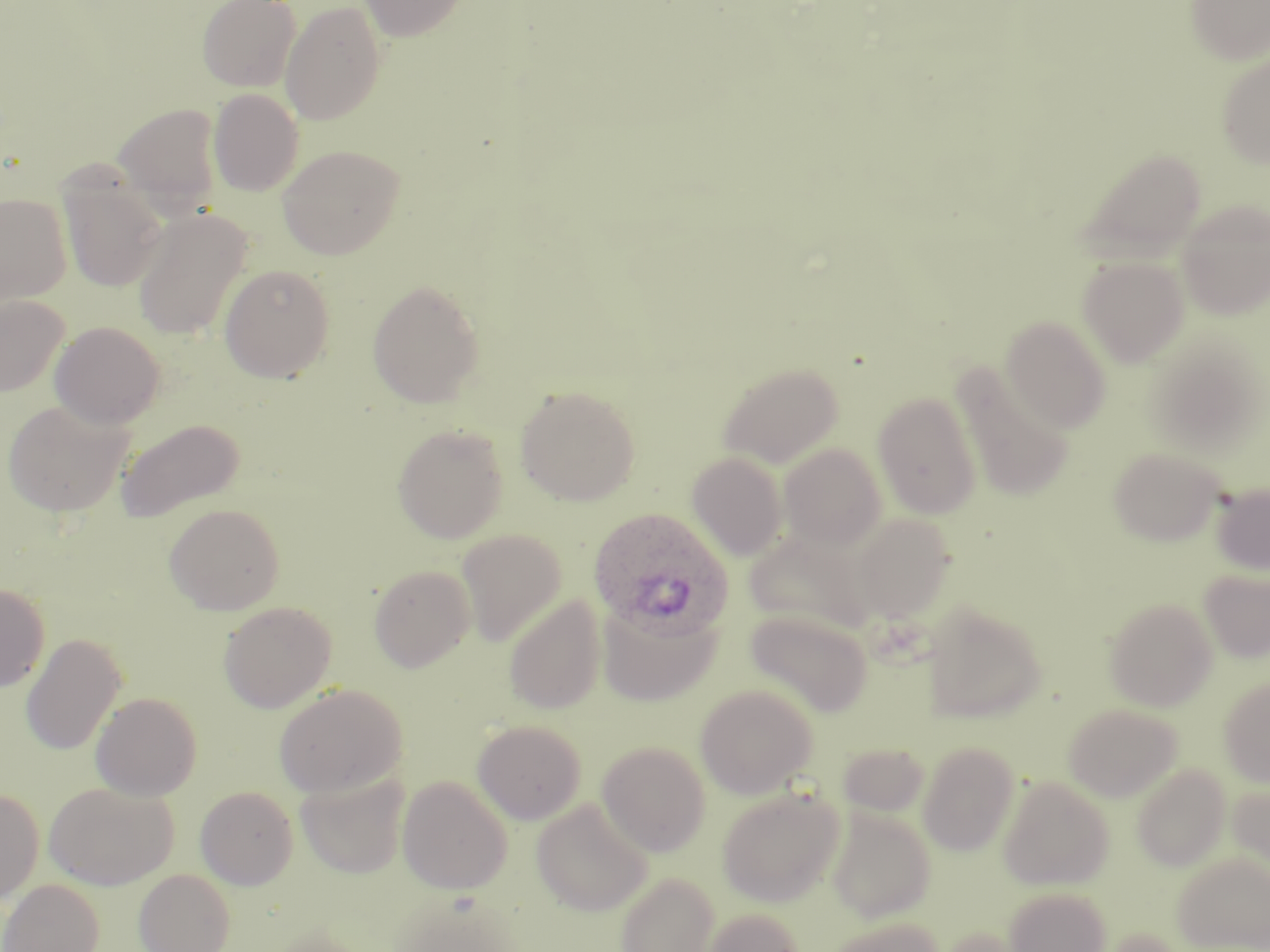

Summary:
  - Coordinate format: approximate bounding boxes as (x1, y1, x2, y2) in pixels
  - Uninfected red blood cell locations: (197, 0, 301, 91), (359, 0, 469, 41), (1185, 0, 1270, 65), (280, 1, 386, 125), (1216, 51, 1270, 169), (208, 89, 304, 196), (112, 102, 224, 212), (278, 144, 406, 259), (1076, 147, 1207, 262), (59, 174, 167, 293), (0, 193, 72, 305), (1177, 199, 1269, 320), (132, 208, 251, 341), (1078, 256, 1189, 367), (219, 263, 335, 382), (367, 279, 485, 407), (0, 294, 69, 396), (1002, 316, 1111, 433), (50, 321, 165, 429), (717, 361, 844, 469), (951, 361, 1074, 502), (515, 384, 640, 506), (873, 392, 981, 519), (2, 400, 135, 518), (115, 418, 245, 523), (392, 425, 508, 543), (779, 443, 887, 549), (1109, 446, 1226, 546), (686, 451, 787, 560), (1211, 482, 1270, 576), (164, 503, 285, 615), (852, 514, 956, 623), (456, 529, 567, 646), (369, 564, 476, 672), (1200, 570, 1270, 663), (0, 583, 50, 692), (503, 596, 606, 715), (1104, 598, 1217, 711), (218, 601, 337, 713), (598, 601, 722, 706), (922, 603, 1047, 723), (746, 610, 873, 717), (20, 633, 126, 756), (1219, 677, 1270, 786), (273, 683, 408, 798), (695, 684, 818, 799), (90, 692, 202, 801), (1063, 704, 1182, 801), (472, 719, 587, 824), (596, 741, 711, 856), (917, 741, 1021, 856), (836, 742, 931, 819), (1131, 763, 1231, 871), (296, 771, 410, 879), (397, 775, 512, 894), (997, 776, 1114, 891), (44, 781, 178, 890), (1228, 781, 1270, 879), (195, 786, 298, 889), (717, 786, 844, 907), (0, 788, 44, 905), (531, 798, 653, 916), (826, 807, 936, 921), (1172, 851, 1270, 950), (134, 868, 235, 952), (615, 872, 720, 952), (0, 878, 105, 952), (1004, 886, 1111, 952), (699, 907, 805, 952), (823, 916, 945, 952)
  - Plasmodium ovale-infected red blood cell locations: (588, 507, 734, 642)
  - Slide-level diagnosis: Plasmodium ovale
  - Field of view: one of a larger specimen
  - Image size: 1270×952 pixels
  - Stain: May-Grünwald-Giemsa
  - Preparation: thin blood film
  - Magnification: 1000x
  - Modality: light microscopy